Assess for malaria.
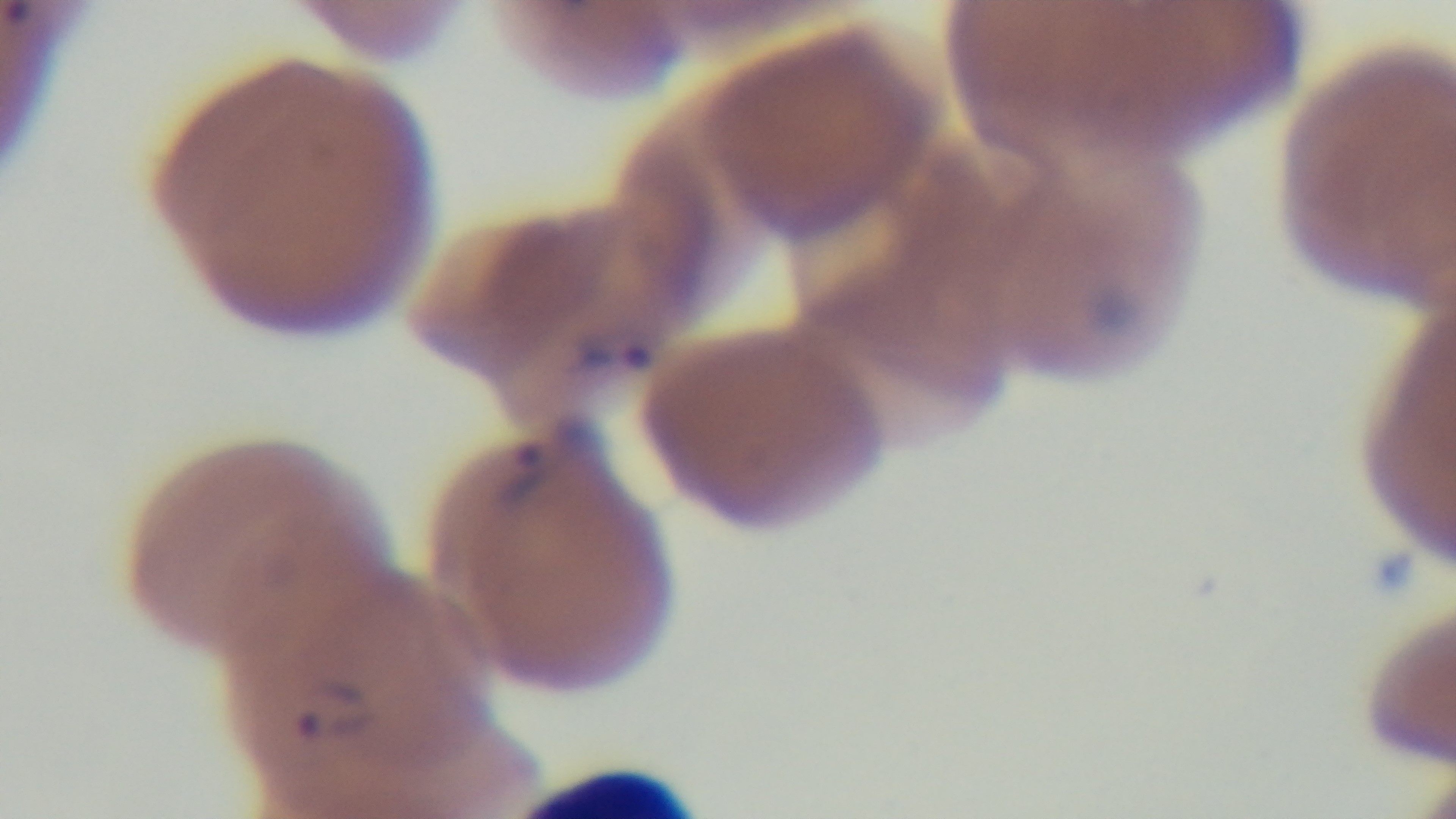

It is infected.

Summary:
  - Objective: 100x oil immersion
  - Capture: mounted 4K digital camera
  - Field of view: single
  - Stain: Giemsa
  - Modality: light microscopy
  - Preparation: thin